Classify this cell by malaria status.
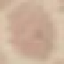
It is uninfected.

Summary:
  - Image type: automatically extracted cell patch, resized to 64 × 64 pixels
  - Capture: smartphone camera at the microscope eyepiece
  - Stain: Giemsa
  - Preparation: thin smear